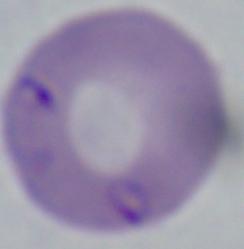
Captured at 1000x magnification. A Babesia parasite is seen. Micrograph.